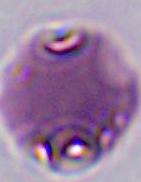 Micrograph. A Plasmodium parasite is shown. 400x or 1000x magnification.